Outline each blood parasite and name the species.
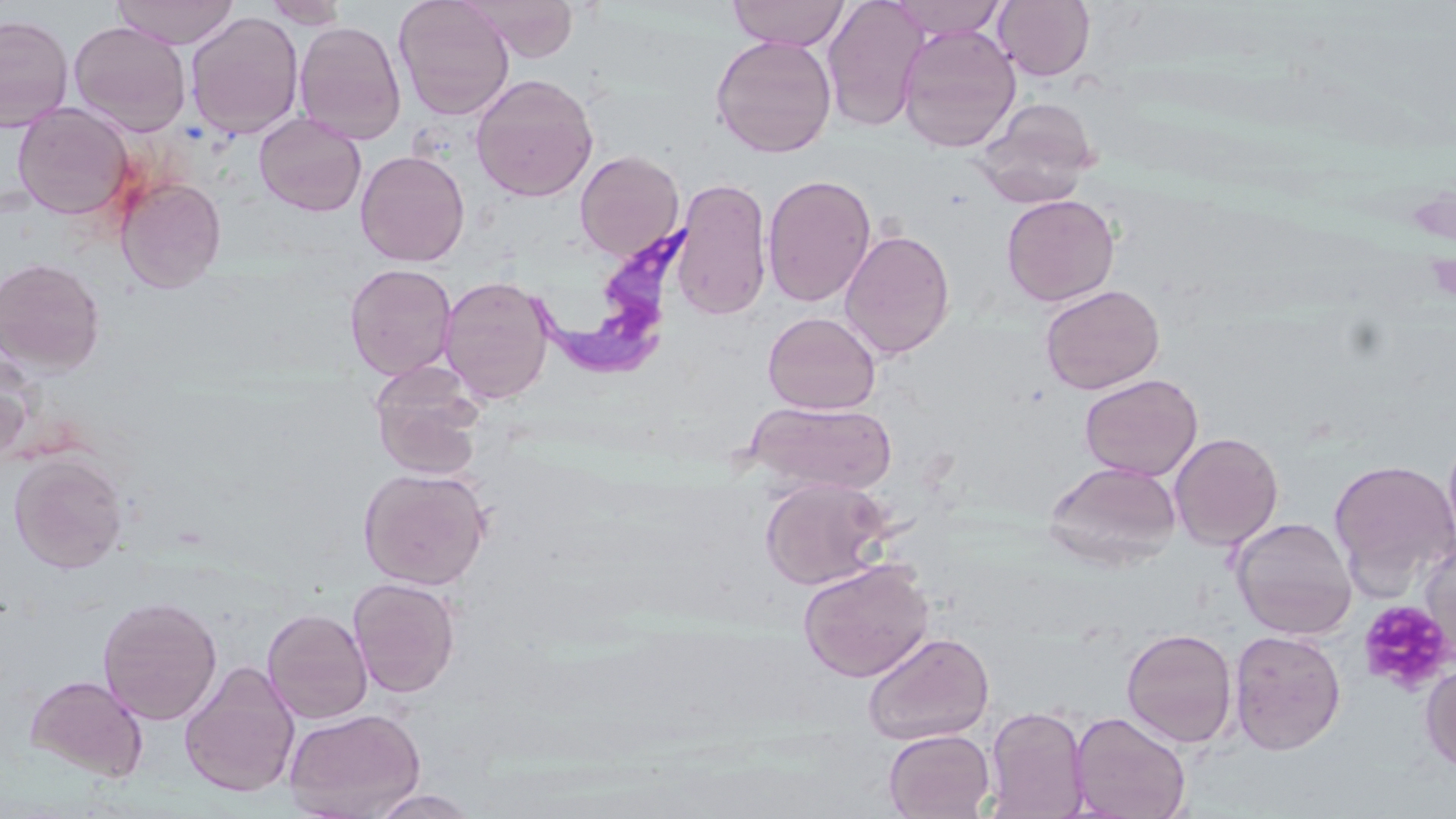
Approximate bounding boxes as named x1/y1/x2/y2 corners in pixels.
Trypanosoma brucei: (x1=520, y1=216, x2=711, y2=381).
No Plasmodium falciparum, Plasmodium ovale, Plasmodium malariae, Plasmodium vivax, or Babesia divergens observed.

Uninfected red blood cell locations: (x1=112, y1=0, x2=240, y2=49), (x1=263, y1=0, x2=350, y2=28), (x1=394, y1=0, x2=514, y2=120), (x1=469, y1=0, x2=579, y2=61), (x1=727, y1=0, x2=850, y2=50), (x1=822, y1=0, x2=928, y2=132), (x1=886, y1=0, x2=1007, y2=39), (x1=994, y1=1, x2=1095, y2=81), (x1=185, y1=11, x2=304, y2=140), (x1=0, y1=13, x2=74, y2=132), (x1=69, y1=20, x2=192, y2=136), (x1=294, y1=21, x2=406, y2=144), (x1=896, y1=24, x2=1021, y2=153), (x1=710, y1=35, x2=837, y2=158), (x1=470, y1=73, x2=598, y2=202), (x1=975, y1=98, x2=1100, y2=207), (x1=12, y1=103, x2=136, y2=222), (x1=254, y1=112, x2=367, y2=217), (x1=355, y1=150, x2=470, y2=267), (x1=575, y1=151, x2=685, y2=261), (x1=762, y1=173, x2=877, y2=308), (x1=115, y1=175, x2=226, y2=292), (x1=670, y1=178, x2=773, y2=320), (x1=1001, y1=194, x2=1120, y2=306), (x1=839, y1=228, x2=955, y2=360), (x1=0, y1=257, x2=106, y2=374), (x1=344, y1=263, x2=457, y2=379), (x1=439, y1=275, x2=556, y2=404), (x1=1040, y1=284, x2=1165, y2=395), (x1=762, y1=311, x2=881, y2=415), (x1=0, y1=349, x2=37, y2=462), (x1=369, y1=362, x2=486, y2=479), (x1=1079, y1=374, x2=1203, y2=481), (x1=746, y1=400, x2=898, y2=495), (x1=1443, y1=427, x2=1456, y2=556), (x1=1169, y1=432, x2=1284, y2=551), (x1=8, y1=452, x2=128, y2=573), (x1=1329, y1=459, x2=1456, y2=594), (x1=1045, y1=461, x2=1181, y2=568), (x1=358, y1=467, x2=491, y2=590), (x1=760, y1=476, x2=892, y2=591), (x1=1231, y1=516, x2=1357, y2=640), (x1=1418, y1=538, x2=1456, y2=668), (x1=798, y1=558, x2=934, y2=682), (x1=348, y1=578, x2=461, y2=697), (x1=97, y1=595, x2=222, y2=725), (x1=262, y1=607, x2=373, y2=724), (x1=1121, y1=628, x2=1238, y2=748), (x1=1229, y1=629, x2=1346, y2=755), (x1=862, y1=631, x2=994, y2=745), (x1=179, y1=662, x2=301, y2=799), (x1=1420, y1=663, x2=1456, y2=775), (x1=24, y1=673, x2=149, y2=782), (x1=984, y1=705, x2=1090, y2=819), (x1=284, y1=707, x2=426, y2=818), (x1=1069, y1=711, x2=1192, y2=818), (x1=883, y1=729, x2=995, y2=819), (x1=366, y1=789, x2=480, y2=818). Platelet locations: (x1=1425, y1=255, x2=1456, y2=301), (x1=1358, y1=600, x2=1454, y2=694). Slide-level diagnosis: Trypanosoma brucei. Thin blood film. Light microscopy. Captured at 1000x magnification. May-Grünwald-Giemsa-stained preparation. One field of a larger specimen. Image is 1456×819 pixels.